Outline each uninfected red blood cell.
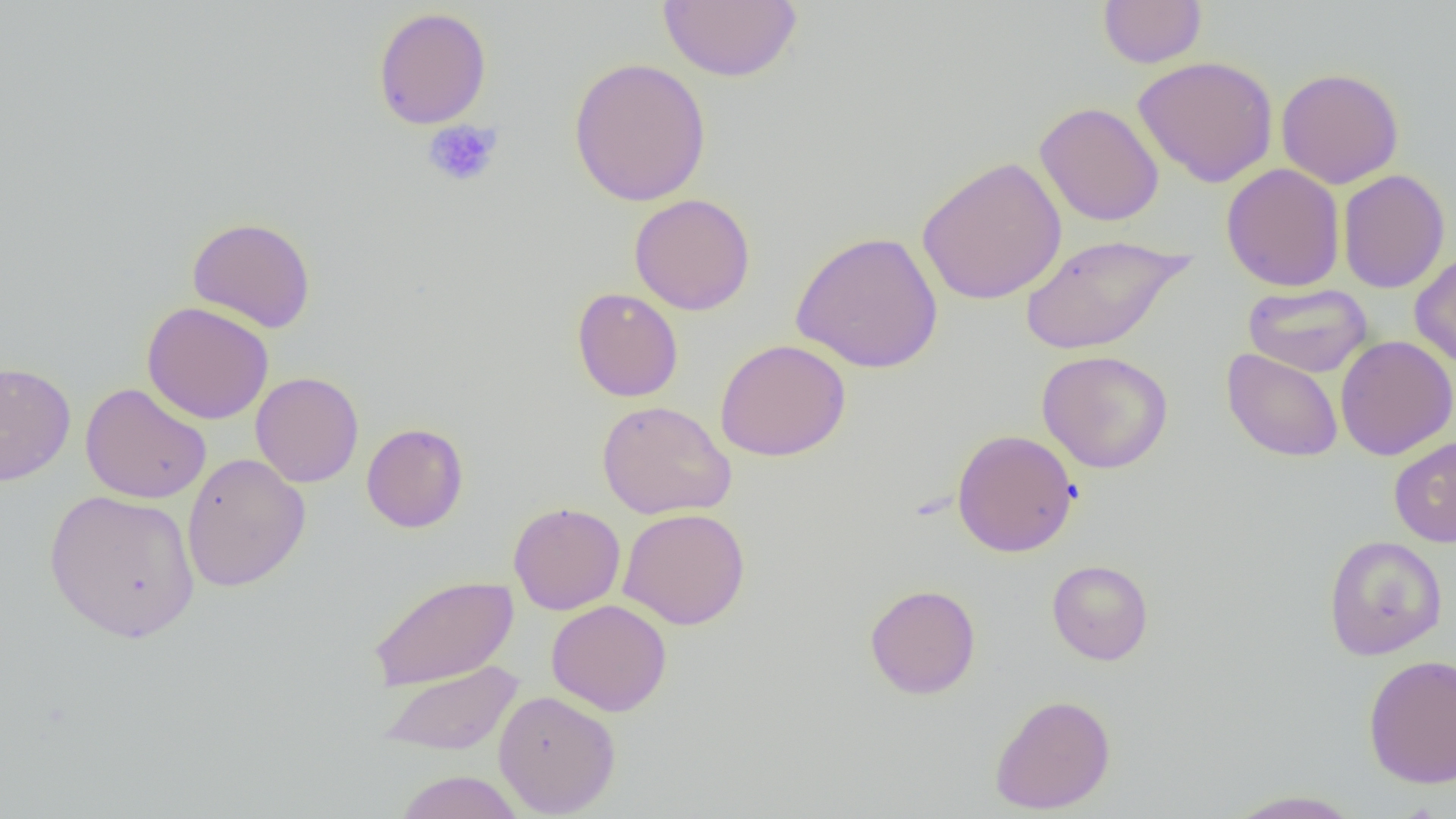
Approximate bounding boxes as named x1/y1/x2/y2 corners in pixels.
Uninfected red blood cells: (x1=659, y1=0, x2=803, y2=82), (x1=1097, y1=0, x2=1208, y2=68), (x1=373, y1=6, x2=492, y2=130), (x1=1133, y1=55, x2=1279, y2=188), (x1=568, y1=57, x2=712, y2=207), (x1=1275, y1=67, x2=1405, y2=189), (x1=1034, y1=102, x2=1165, y2=227), (x1=916, y1=155, x2=1067, y2=306), (x1=1221, y1=163, x2=1345, y2=291), (x1=1337, y1=169, x2=1451, y2=294), (x1=629, y1=193, x2=756, y2=315), (x1=187, y1=217, x2=316, y2=333), (x1=790, y1=230, x2=944, y2=374), (x1=1020, y1=233, x2=1192, y2=355), (x1=1409, y1=250, x2=1456, y2=370), (x1=1243, y1=283, x2=1372, y2=377), (x1=571, y1=287, x2=683, y2=402), (x1=142, y1=301, x2=274, y2=425), (x1=1335, y1=335, x2=1456, y2=461), (x1=715, y1=339, x2=852, y2=462), (x1=1222, y1=348, x2=1343, y2=462), (x1=1037, y1=350, x2=1174, y2=473), (x1=0, y1=361, x2=75, y2=487), (x1=251, y1=371, x2=364, y2=488), (x1=80, y1=382, x2=212, y2=504), (x1=597, y1=400, x2=736, y2=520), (x1=361, y1=422, x2=469, y2=533), (x1=951, y1=429, x2=1079, y2=558), (x1=1389, y1=437, x2=1456, y2=547), (x1=181, y1=452, x2=311, y2=592), (x1=44, y1=488, x2=200, y2=643), (x1=508, y1=502, x2=626, y2=615), (x1=618, y1=507, x2=750, y2=630), (x1=1323, y1=534, x2=1447, y2=659), (x1=1347, y1=534, x2=1453, y2=787), (x1=1047, y1=559, x2=1154, y2=665), (x1=367, y1=574, x2=518, y2=691), (x1=865, y1=583, x2=981, y2=699), (x1=546, y1=598, x2=672, y2=717), (x1=1362, y1=654, x2=1456, y2=789), (x1=379, y1=661, x2=523, y2=755), (x1=493, y1=689, x2=621, y2=817), (x1=989, y1=693, x2=1116, y2=815), (x1=395, y1=770, x2=524, y2=819), (x1=1222, y1=789, x2=1366, y2=818).

Summary:
  - Platelet locations: (x1=423, y1=120, x2=503, y2=188)
  - Slide-level diagnosis: negative for blood parasites
  - Image size: 1456×819 pixels
  - Magnification: 1000x
  - Preparation: thin blood film
  - Field of view: one of a larger specimen
  - Modality: optical microscopy